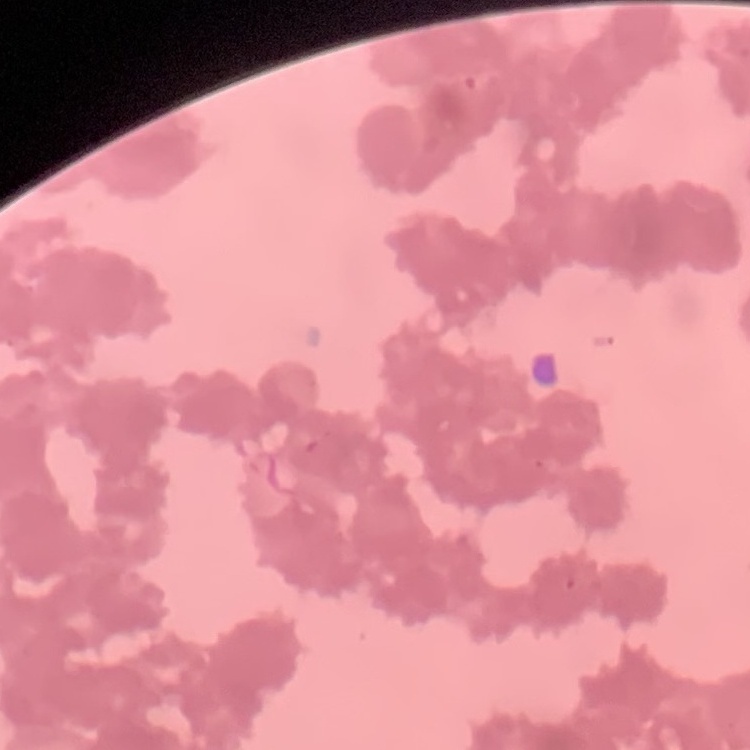 The red blood cells show rouleaux formation. Thin blood smear. Field's or Giemsa stain. Square crop of a larger photomicrograph.